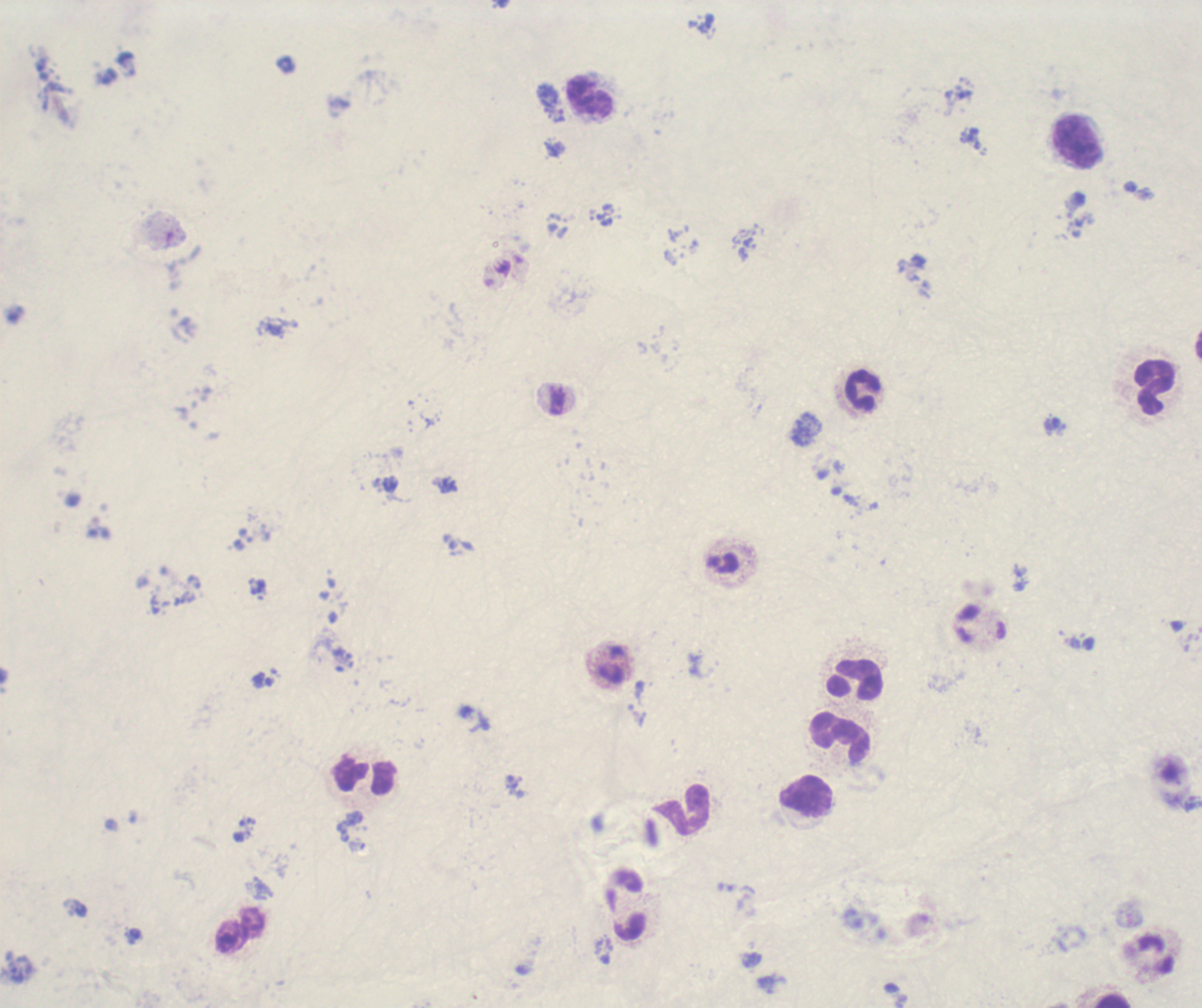
coordinate format = approximate centers as (x, y) in pixels
leukocyte locations = (590, 98), (1079, 141), (1155, 386), (863, 391), (855, 679), (840, 739), (364, 776), (806, 797), (684, 808), (627, 906), (241, 931), (1113, 1001)
magnification = 100x
background quality = unsatisfactory
field of view = one from this slide
stain = Romanowsky
image size = 1202×1008 pixels
context = previously used in a real diagnosis
result = no malaria parasites detected
preparation = thick smear of blood